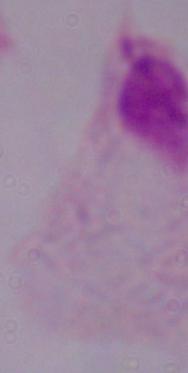

identification = trichomonad
modality = micrograph
magnification = 1000x